Name the blood parasite species.
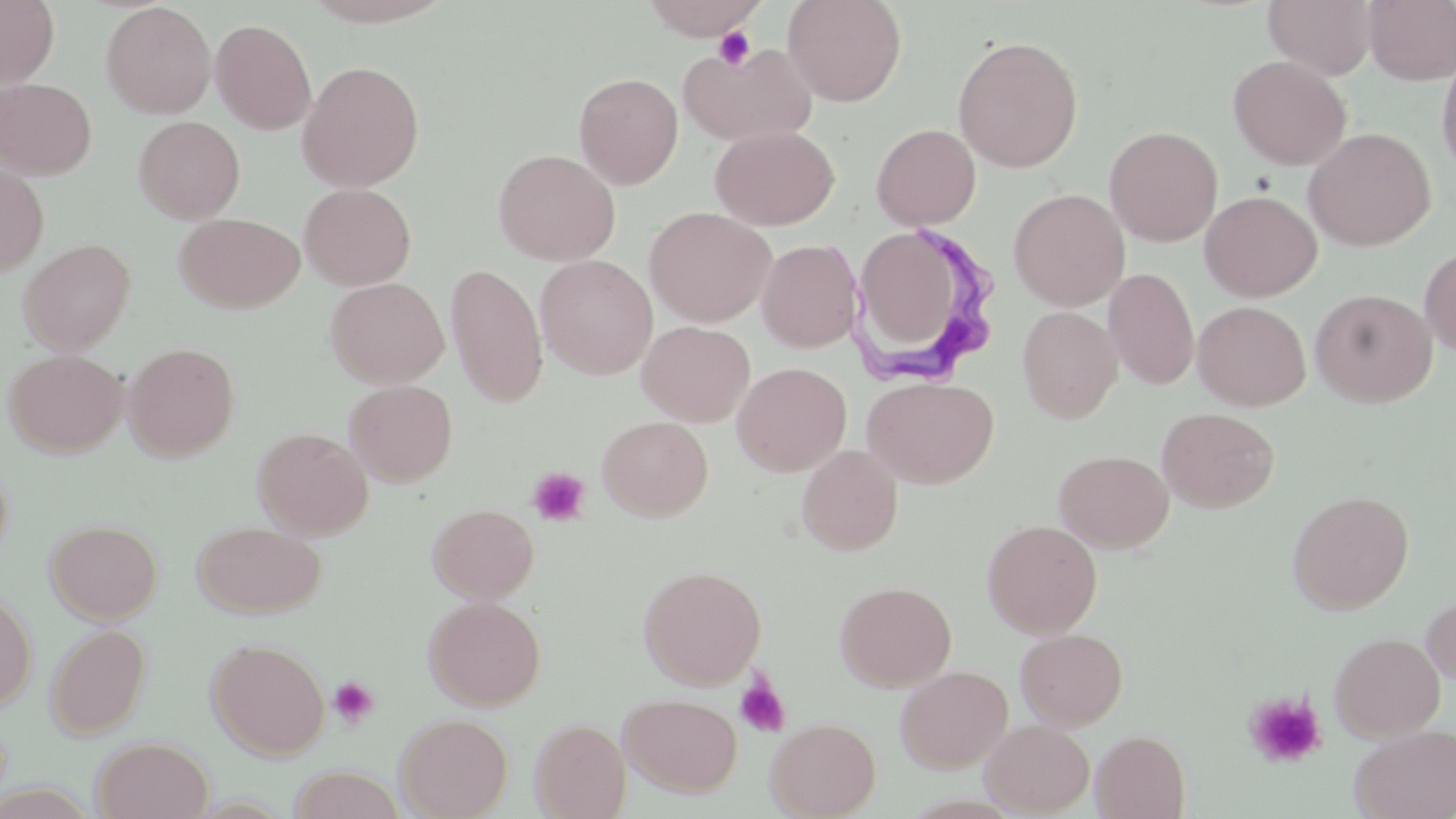
Trypanosoma brucei.

Summary:
  - Coordinate format: approximate bounding boxes as (x1, y1, x2, y2) in pixels
  - Uninfected red blood cell locations: (0, 0, 59, 88), (639, 0, 770, 40), (782, 0, 908, 107), (1262, 0, 1378, 80), (1362, 0, 1456, 85), (100, 2, 216, 119), (210, 18, 317, 134), (952, 35, 1084, 172), (679, 42, 818, 146), (1436, 48, 1456, 179), (1228, 54, 1351, 170), (297, 60, 424, 192), (574, 72, 684, 189), (0, 77, 97, 179), (133, 116, 245, 223), (871, 124, 981, 230), (710, 125, 839, 230), (1104, 125, 1224, 246), (1302, 127, 1436, 250), (493, 149, 620, 266), (0, 163, 48, 278), (300, 183, 416, 290), (1008, 189, 1129, 311), (1200, 190, 1322, 301), (644, 206, 775, 327), (174, 212, 305, 313), (18, 238, 136, 355), (865, 238, 956, 342), (757, 239, 863, 353), (1419, 244, 1456, 358), (535, 255, 658, 379), (445, 263, 548, 407), (1103, 268, 1200, 390), (325, 277, 448, 388), (1310, 288, 1437, 407), (1192, 301, 1311, 410), (1017, 306, 1122, 424), (637, 320, 755, 426), (122, 341, 240, 461), (4, 349, 127, 458), (732, 362, 852, 476), (862, 376, 999, 488), (344, 380, 458, 486), (1157, 407, 1279, 513), (596, 416, 713, 521), (252, 427, 373, 539), (796, 445, 903, 555), (1055, 449, 1173, 553), (1286, 490, 1414, 613), (427, 503, 539, 603), (45, 518, 162, 624), (982, 519, 1102, 637), (191, 520, 327, 618), (638, 564, 767, 689), (834, 581, 957, 691), (0, 589, 36, 712), (1421, 592, 1456, 690), (423, 596, 546, 710), (45, 623, 152, 739), (1015, 628, 1128, 730), (1329, 631, 1446, 741), (206, 638, 330, 760), (895, 665, 1013, 773), (620, 693, 743, 797), (395, 712, 513, 819), (529, 712, 742, 814), (766, 717, 881, 819), (530, 718, 631, 818), (980, 719, 1095, 816), (1350, 724, 1456, 819), (1091, 730, 1190, 818), (92, 736, 213, 819), (285, 766, 405, 819)
  - Trypanosoma brucei locations: (850, 220, 994, 382)
  - Platelet locations: (712, 26, 757, 71), (527, 466, 591, 526), (734, 674, 791, 738), (328, 675, 380, 729), (1242, 690, 1328, 769)
  - Modality: light microscopy
  - Stain: May-Grünwald-Giemsa
  - Magnification: 1000x
  - Field of view: one of a larger specimen
  - Preparation: thin blood film
  - Image size: 1456×819 pixels